Report the malaria status of this cell.
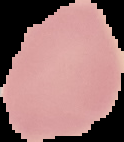

It is uninfected.

preparation = thin blood smear
image size = 124×142 pixels
image type = cell region segmented out of the field of view; surrounding area masked to black